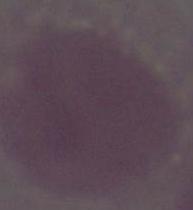
Summary:
  - Magnification: 1000x
  - Modality: micrograph
  - Identification: erythrocyte